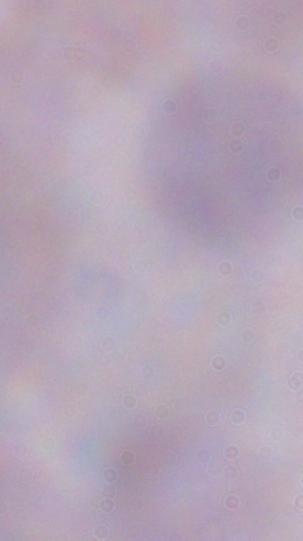

magnification = 1000x
modality = photomicrograph
identification = trypanosome